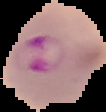
{
  "image_size": "106×112 pixels",
  "image_type": "cell region segmented out of the field of view; surrounding area masked to black",
  "preparation": "thin blood film",
  "malaria_status": "parasitized"
}